Report the malaria status of this cell.
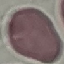
Uninfected.

capture = smartphone camera at the microscope eyepiece
image type = automatically extracted cell patch, resized to 64 × 64 pixels
preparation = thin blood film
stain = Giemsa